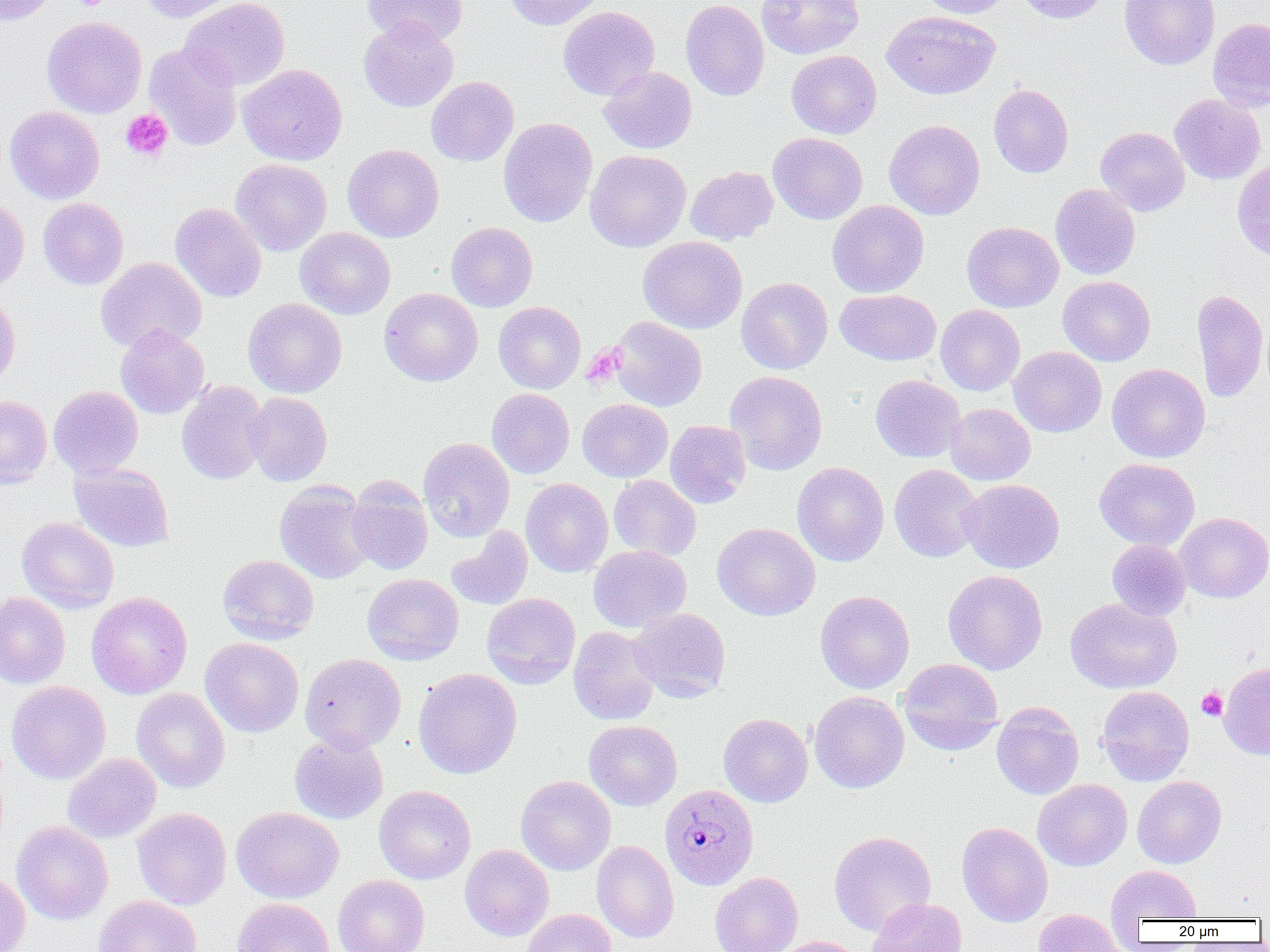
slide-level diagnosis = Plasmodium malariae
modality = light microscopy
uninfected red blood cell locations = approximate bounding boxes as [x1, y1, x2, y2] in pixels: [1, 0, 58, 27], [138, 0, 246, 23], [180, 0, 290, 90], [362, 0, 468, 46], [504, 0, 607, 30], [681, 0, 769, 101], [756, 0, 864, 60], [916, 0, 1011, 19], [1012, 0, 1111, 24], [1120, 0, 1220, 69], [558, 6, 659, 100], [882, 10, 1000, 99], [42, 16, 147, 119], [1208, 17, 1270, 112], [359, 18, 458, 112], [144, 42, 243, 150], [786, 50, 882, 139], [237, 64, 348, 166], [598, 67, 697, 153], [426, 76, 518, 166], [988, 84, 1074, 178], [1169, 94, 1266, 184], [5, 106, 105, 204], [498, 117, 597, 228], [884, 119, 984, 220], [1095, 126, 1189, 216], [768, 133, 867, 224], [342, 144, 444, 242], [585, 149, 691, 252], [230, 158, 332, 256], [1232, 159, 1270, 263], [685, 166, 778, 244], [1050, 184, 1140, 280], [0, 197, 29, 295], [38, 197, 129, 289], [827, 200, 929, 298], [170, 202, 266, 302], [446, 222, 537, 312], [962, 222, 1064, 312], [294, 227, 395, 320], [638, 236, 747, 333], [95, 257, 207, 354], [1058, 276, 1155, 366], [736, 277, 833, 374], [379, 288, 483, 386], [834, 289, 941, 365], [1191, 289, 1269, 403], [0, 292, 20, 392], [243, 298, 347, 398], [493, 302, 585, 393], [935, 304, 1025, 396], [611, 316, 707, 411], [115, 324, 210, 419], [1009, 346, 1106, 437], [1107, 363, 1210, 462], [725, 371, 827, 474], [870, 375, 965, 463], [176, 381, 271, 485], [48, 386, 143, 478], [487, 388, 574, 478], [245, 392, 332, 486], [0, 396, 52, 488], [577, 399, 673, 482], [945, 403, 1035, 485], [665, 420, 751, 508], [418, 438, 515, 542], [1094, 458, 1200, 550], [69, 462, 174, 552], [792, 462, 889, 567], [889, 464, 984, 562], [608, 475, 701, 561], [347, 478, 433, 575], [521, 478, 613, 577], [959, 478, 1064, 573], [274, 480, 374, 585], [1174, 512, 1270, 602], [17, 517, 119, 613], [712, 522, 820, 620], [446, 527, 533, 611], [1107, 540, 1191, 621], [588, 545, 691, 632], [217, 554, 318, 644], [943, 570, 1047, 675], [362, 573, 464, 664], [815, 590, 914, 694], [0, 592, 70, 689], [86, 592, 192, 699], [482, 593, 580, 689], [1066, 598, 1182, 694], [629, 608, 730, 701], [568, 626, 661, 725], [201, 637, 304, 738], [300, 653, 406, 752], [898, 658, 1003, 756], [1219, 662, 1270, 760], [413, 668, 522, 779], [6, 680, 111, 784], [1097, 685, 1194, 786], [132, 688, 230, 793], [809, 691, 909, 793], [991, 701, 1084, 799], [718, 713, 813, 807], [584, 720, 682, 811], [289, 731, 388, 824], [63, 753, 161, 843], [515, 775, 616, 875], [1132, 776, 1226, 868], [1033, 779, 1132, 871], [373, 785, 475, 884], [132, 807, 232, 909], [231, 807, 343, 903], [12, 821, 113, 925], [957, 822, 1053, 926], [829, 831, 936, 936], [592, 841, 678, 942], [460, 844, 554, 941], [1107, 865, 1202, 923], [0, 871, 31, 952], [710, 872, 803, 952], [333, 875, 430, 952], [92, 895, 202, 952], [867, 897, 967, 952], [233, 898, 334, 952], [521, 908, 616, 952], [1034, 909, 1127, 952], [770, 936, 866, 952]
preparation = thin blood smear
field of view = one of a larger specimen
Plasmodium malariae-infected red blood cell locations = approximate bounding boxes as [x1, y1, x2, y2] in pixels: [660, 784, 759, 889]
platelet locations = approximate bounding boxes as [x1, y1, x2, y2] in pixels: [69, 0, 111, 10], [120, 109, 173, 162], [582, 343, 625, 387], [1196, 687, 1227, 720]
magnification = 1000x
image size = 1270×952 pixels